Classify this cell by malaria status.
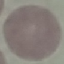
It is uninfected.

{
  "stain": "Giemsa",
  "image_type": "cell patch, automatically extracted from a larger field of view and resized to 64 × 64 pixels",
  "capture": "smartphone through the microscope eyepiece",
  "preparation": "thin smear"
}